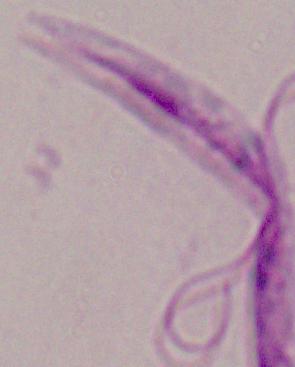

A Leishmania parasite is shown. 1000x magnification. Photomicrograph.